Assess this cell for malaria.
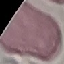

Uninfected.

Summary:
  - Preparation: thin blood film
  - Capture: smartphone camera at the microscope eyepiece
  - Stain: Giemsa
  - Image type: automatically extracted cell patch, resized to 64 × 64 pixels